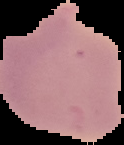

Summary:
  - Image type: segmented cell region with the area outside set to black
  - Result: no malaria parasites detected
  - Preparation: thin blood film
  - Image size: 124×145 pixels